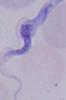
modality: photomicrograph
magnification: 1000x
identification: trypanosome